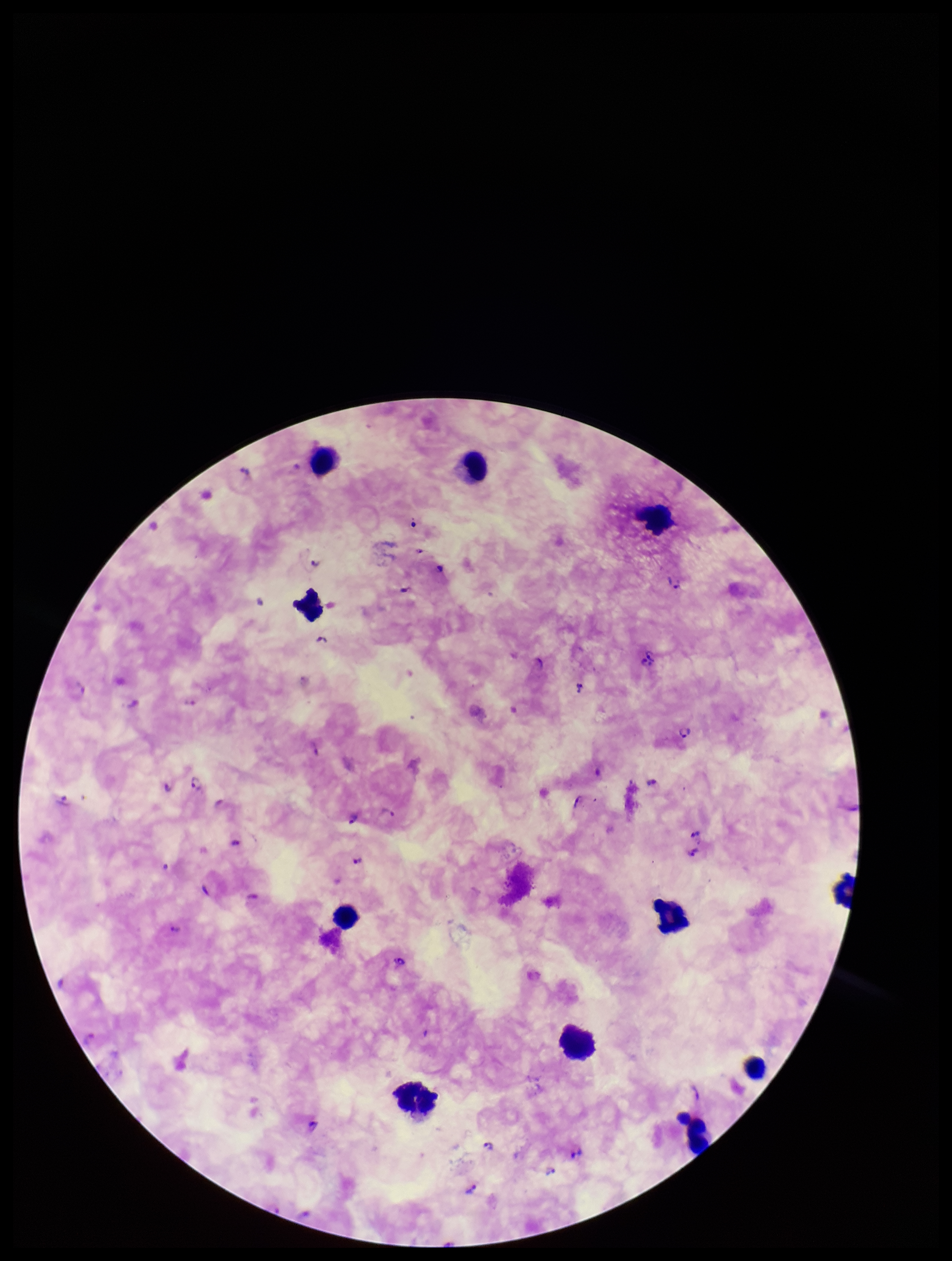

Parasite count: 31. Plasmodium parasites: seen. Leukocyte count: 11. One field from this slide. Image is 952×1261 pixels. Patient malaria status: positive. Species reported for this patient: Plasmodium falciparum. Photographed through the microscope eyepiece with a smartphone camera. Giemsa stain. Preparation: thick blood smear.